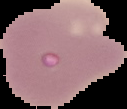
Cell region segmented out of the field of view; the surrounding area is masked to black. From a thin blood film. Image is 127×109 pixels. Malaria status: uninfected.